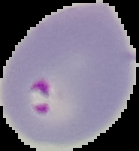
Image is 139×151 pixels. The area outside the segmented cell region is set to black. From a thin blood smear. Result: malaria parasites identified.